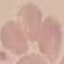
Result: no malaria parasites detected. Cell patch, automatically extracted from a larger field of view and resized to 64 × 64 pixels. Photographed with a smartphone camera at the microscope eyepiece. Thin smear of blood. Giemsa stain.